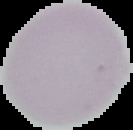
Summary:
  - Image size: 133×130 pixels
  - Preparation: thin blood film
  - Malaria status: uninfected
  - Image type: cell region segmented out of the field of view; surrounding area masked to black